Report the malaria status of this cell.
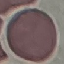
It is uninfected.

Giemsa stain. Cell patch, automatically extracted from a larger field of view and resized to 64 × 64 pixels. Photographed with a smartphone camera at the microscope eyepiece. Thin blood smear.